Comment on the morphology of the red blood cells.
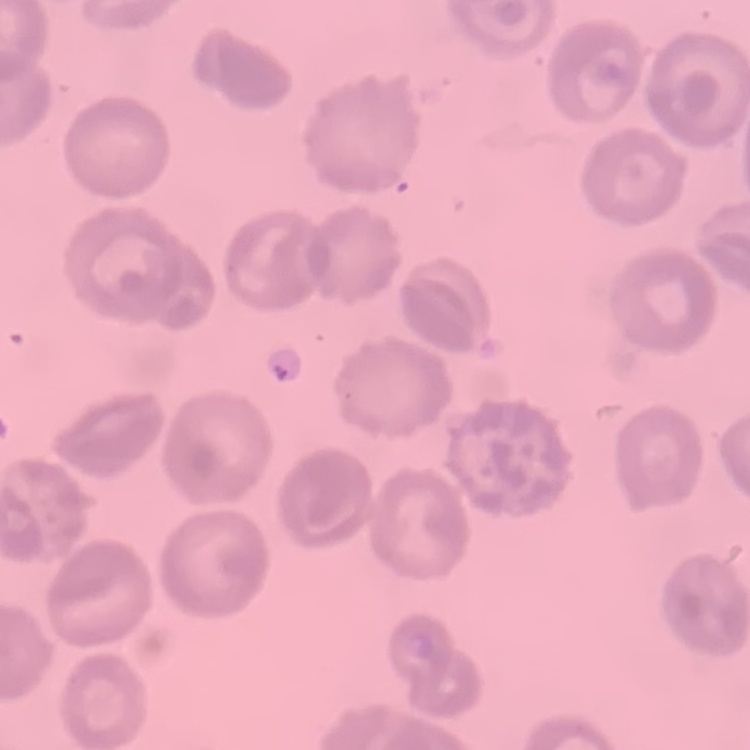
No rouleaux formation.

Summary:
  - Preparation: thin blood smear
  - Image type: one tile cut from a larger photomicrograph
  - Stain: Field's or Giemsa